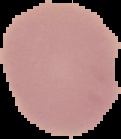

Malaria status: uninfected. Image is 121×139 pixels. From a thin blood smear. The area outside the segmented cell region is set to black.